Classify this cell by malaria status.
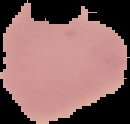

Uninfected.

Summary:
  - Image type: segmented cell region with the area outside set to black
  - Image size: 130×124 pixels
  - Preparation: thin blood film